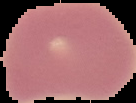
image size = 136×103 pixels
result = no Plasmodium parasites detected
preparation = thin blood film
image type = cell region segmented out of the field of view; surrounding area masked to black